Report the malaria status of this cell.
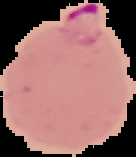
It is parasitized.

preparation = thin blood smear
image size = 136×157 pixels
image type = segmented cell region with the area outside set to black